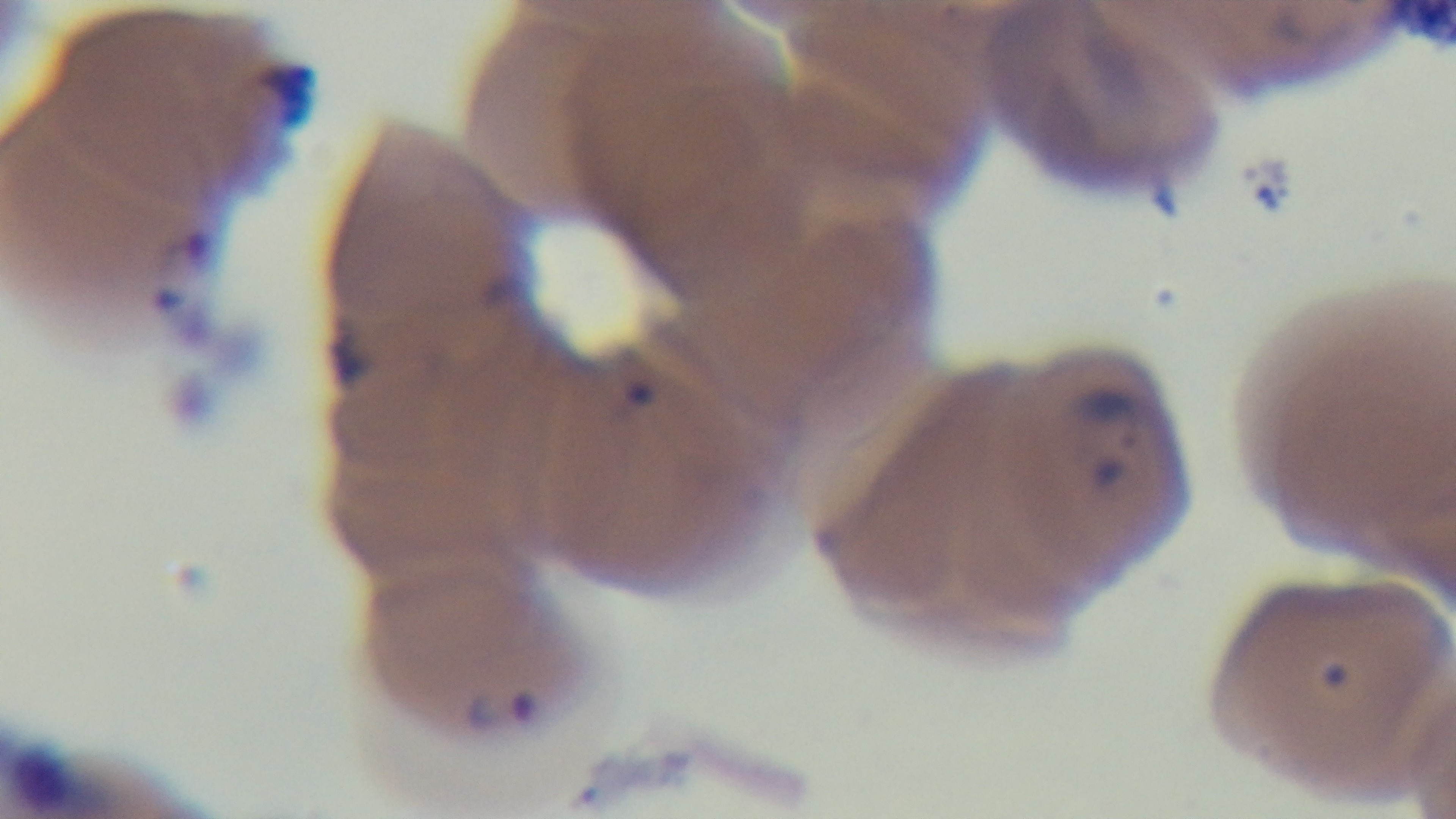 Photomicrograph. Malaria status: positive. Giemsa stain. Preparation: thin smear. One field from the slide. 100x oil-immersion objective. Captured with a mounted 4K digital camera.